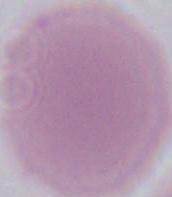
An erythrocyte is shown. Captured at 1000x magnification. Micrograph.